Assess this cell for malaria.
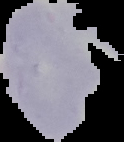

Uninfected.

{
  "image_type": "segmented cell region with the area outside set to black",
  "image_size": "124×142 pixels",
  "preparation": "thin blood smear"
}